State which parasite is depicted.
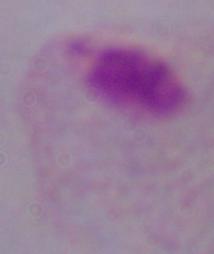

This is a trichomonad.

Summary:
  - Magnification: 1000x
  - Modality: photomicrograph